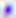 400x magnification. Photomicrograph. Toxoplasma gondii is shown.